Assess this cell for malaria.
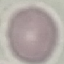
Uninfected.

Summary:
  - Stain: Giemsa
  - Image type: cell patch, automatically extracted from a larger field of view and resized to 64 × 64 pixels
  - Preparation: thin blood smear
  - Capture: smartphone camera at the microscope eyepiece